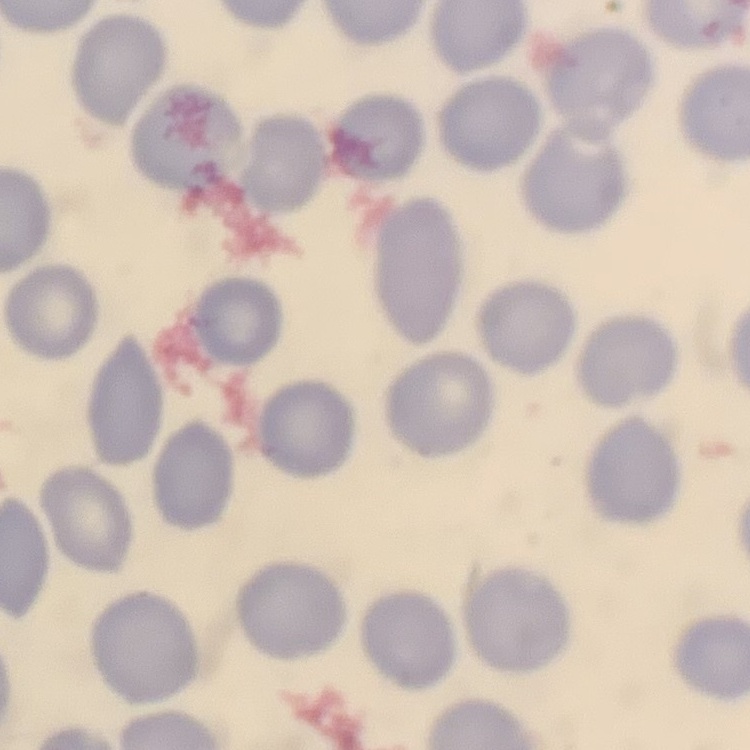

Summary:
  - Erythrocyte morphology: no rouleaux formation
  - Preparation: thin blood film
  - Image type: square crop of a larger photomicrograph
  - Stain: Field's or Giemsa